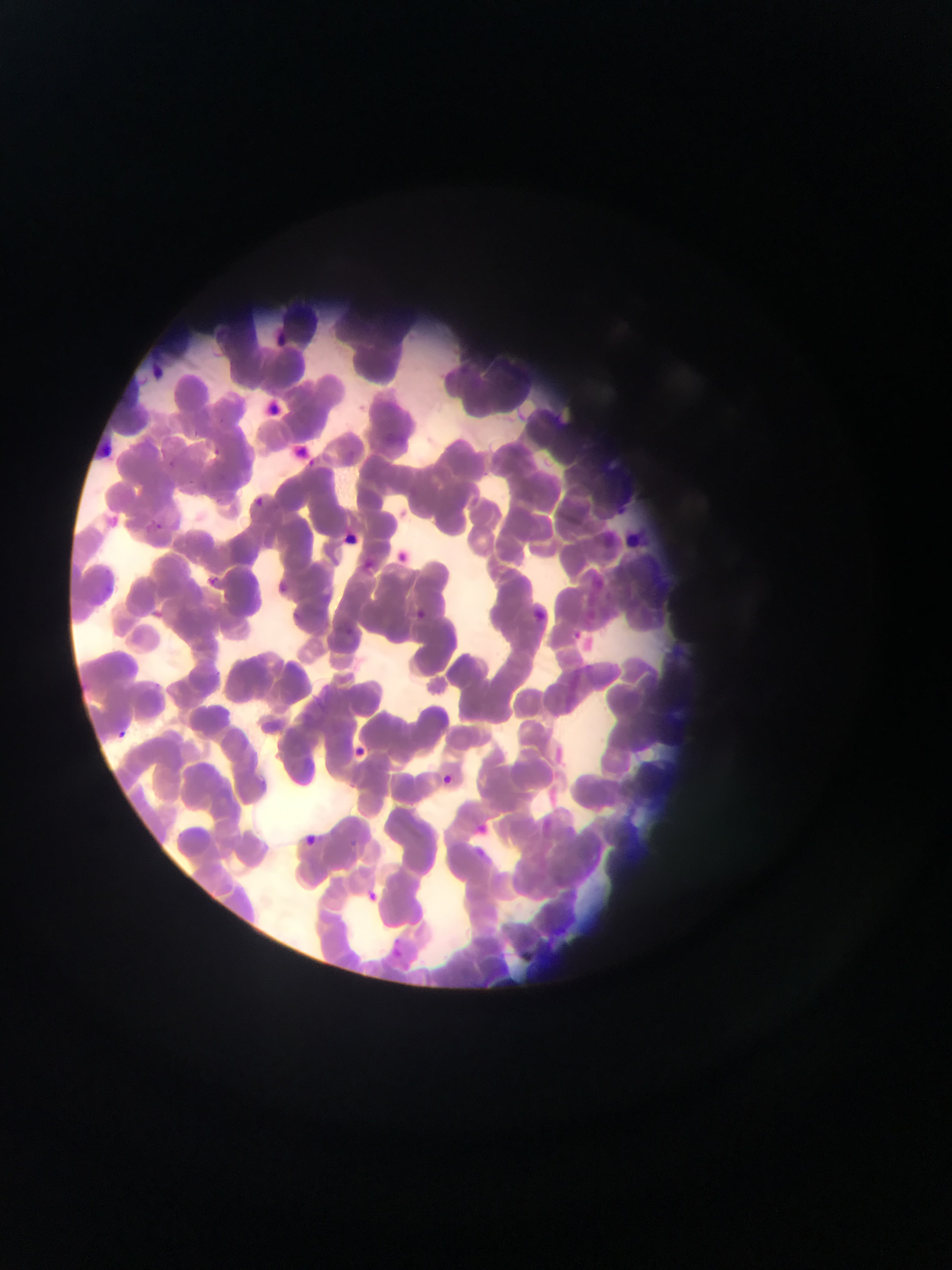
malaria_parasite_locations: 'approximate bounding boxes as left top right bottom in pixels: 278 334 288 345; 153 364 170 383; 267 398 280 415; 189 426 205 442; 299 440 315 459; 213 443 225 459; 161 459 185 472; 229 485 269 520; 152 517 168 528; 341 533 365 549; 399 549 409 565; 363 560 381 575; 206 576 234 595; 99 577 124 596; 274 581 289 593; 530 606 553 625; 149 607 165 621; 414 612 429 627; 343 620 359 638; 570 623 586 640; 102 721 141 738; 351 746 368 761; 440 773 451 783; 476 819 489 832; 304 831 315 848; 343 839 359 849; 475 844 495 861; 361 887 378 901; 390 942 403 956'
field_of_view: single
capture: mobile-phone photograph through a microscope
image_size: 952×1270 pixels
country: Ghana
preparation: thin blood smear